Report the malaria status of this cell.
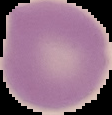

It is uninfected.

Image is 112×115 pixels. From a thin blood smear. Segmented cell region on a black background.